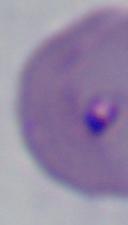

magnification: 1000x
modality: micrograph
identification: Babesia